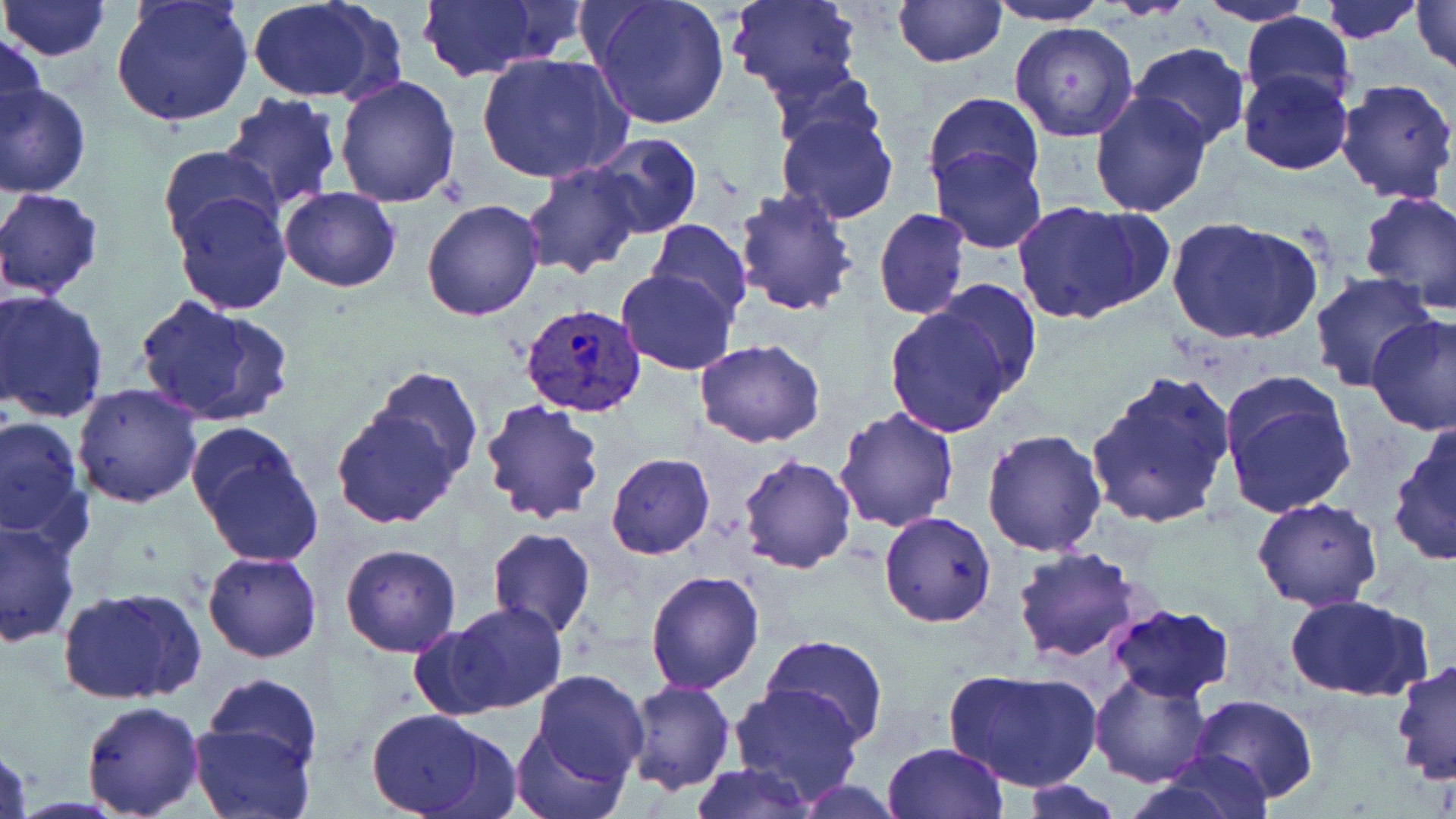
Summary:
  - Coordinate format: approximate bounding boxes as (x1,y1)-(x2,y2) corner pairs in pixels
  - Uninfected red blood cell locations: (1,0)-(111,60), (110,0)-(254,127), (586,0)-(731,129), (724,0)-(863,102), (892,0)-(1007,68), (1317,0)-(1424,42), (1351,0)-(1456,65), (1409,0)-(1455,74), (983,1)-(1111,26), (245,2)-(387,103), (418,2)-(552,80), (1195,2)-(1313,26), (1238,12)-(1356,108), (1009,21)-(1140,142), (1,32)-(44,144), (1130,41)-(1249,149), (477,52)-(630,186), (768,62)-(882,152), (1237,69)-(1353,176), (333,76)-(462,209), (1334,78)-(1456,204), (0,83)-(90,198), (1088,90)-(1213,216), (922,91)-(1045,196), (217,93)-(343,209), (776,112)-(898,224), (588,132)-(702,239), (156,145)-(283,253), (931,146)-(1047,253), (521,162)-(643,279), (279,185)-(401,291), (0,187)-(105,300), (732,188)-(859,317), (1359,189)-(1456,313), (170,191)-(291,314), (421,198)-(544,320), (1012,201)-(1153,323), (873,207)-(970,320), (1165,215)-(1321,346), (647,219)-(751,322), (616,268)-(736,376), (1308,273)-(1438,391), (931,280)-(1041,393), (1,288)-(109,423), (134,293)-(293,430), (884,301)-(1017,437), (1366,315)-(1456,436), (694,339)-(825,449), (370,364)-(484,486), (1220,370)-(1359,519), (1083,371)-(1236,529), (72,383)-(203,507), (478,396)-(606,526), (833,406)-(961,532), (331,409)-(459,528), (1,413)-(85,542), (1388,423)-(1456,566), (189,425)-(325,567), (980,428)-(1108,557), (605,454)-(715,558), (736,454)-(855,573), (1252,496)-(1382,609), (879,511)-(997,628), (0,517)-(80,648), (487,528)-(594,639), (339,543)-(463,657), (1012,545)-(1146,664), (203,550)-(322,662), (645,570)-(765,694), (56,586)-(206,705), (1284,592)-(1428,701), (442,602)-(566,714), (1106,604)-(1236,702), (406,623)-(514,720), (762,635)-(888,744), (1389,658)-(1455,786), (946,667)-(1101,795), (531,670)-(648,781), (1090,672)-(1213,786), (204,673)-(324,774), (624,679)-(735,795), (729,683)-(862,802), (1191,694)-(1318,803), (79,701)-(205,817), (365,708)-(502,818), (187,722)-(316,819), (510,725)-(625,819), (0,738)-(32,819), (881,742)-(1008,819), (1145,749)-(1275,819), (688,763)-(814,818), (790,780)-(906,817), (1015,781)-(1123,817)
  - Plasmodium vivax-infected red blood cell locations: (519,301)-(648,420)
  - Slide-level diagnosis: Plasmodium vivax
  - Field of view: single
  - Image size: 1456×819 pixels
  - Preparation: thin blood smear
  - Modality: optical microscopy
  - Stain: May-Grünwald-Giemsa
  - Magnification: 1000x